Assess this cell for malaria.
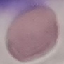
Uninfected.

Giemsa-stained preparation. Photographed with a smartphone camera at the microscope eyepiece. Cell patch, automatically extracted from a larger field of view and resized to 64 × 64 pixels. Thin blood smear.